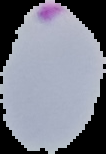 The area outside the segmented cell region is set to black. Image is 106×154 pixels. Malaria status: parasitized. From a thin blood film.